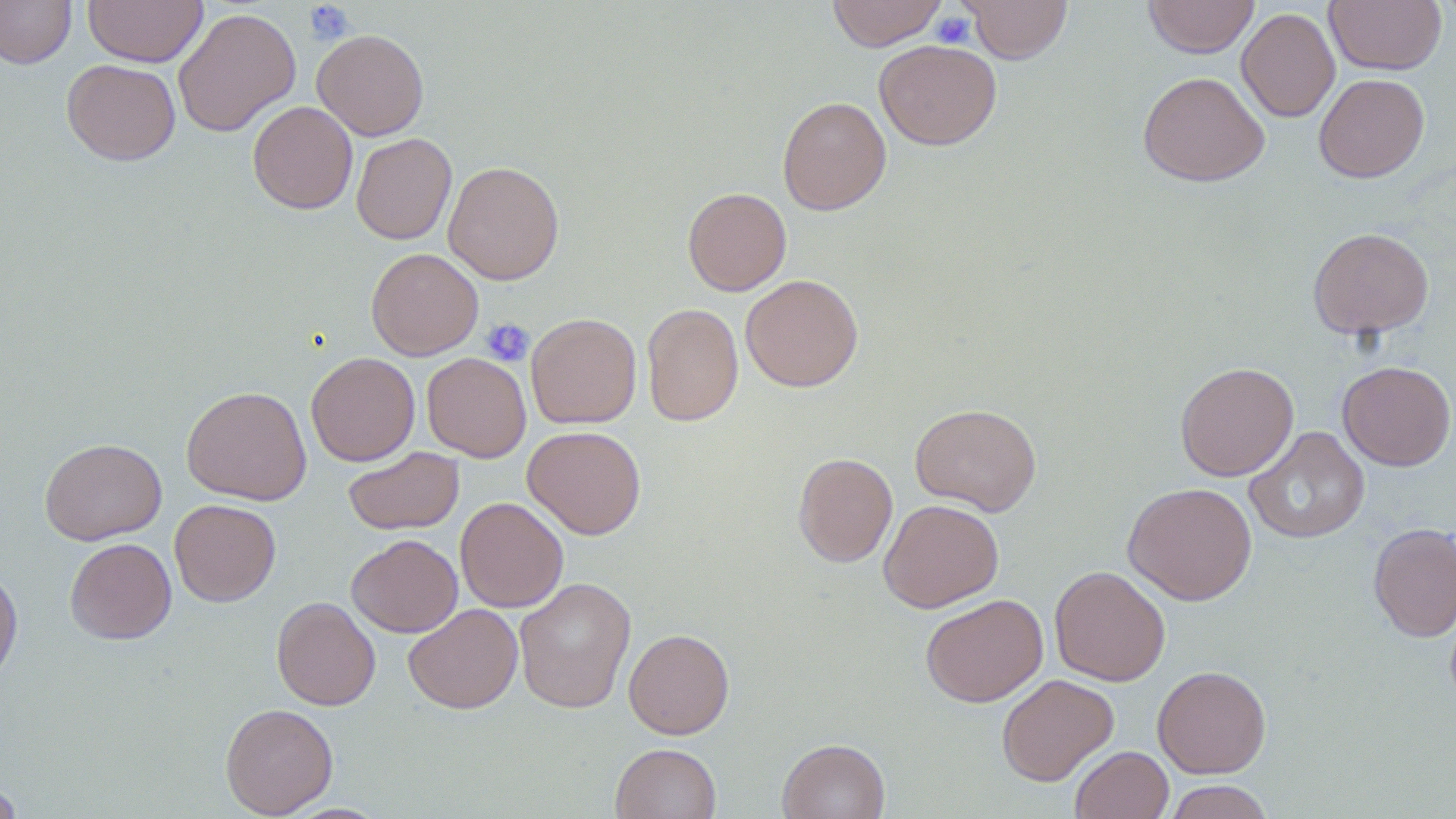
{
  "slide_level_diagnosis": "no evidence of blood parasites",
  "stain": "May-Grünwald-Giemsa",
  "image_size": "1456×819 pixels",
  "modality": "light microscopy",
  "magnification": "1000x",
  "platelet_locations": "approximate bounding boxes as named x1/y1/x2/y2 corners in pixels: (x1=304, y1=1, x2=355, y2=45), (x1=931, y1=11, x2=975, y2=48), (x1=480, y1=318, x2=535, y2=366)",
  "uninfected_red_blood_cell_locations": "approximate bounding boxes as named x1/y1/x2/y2 corners in pixels: (x1=0, y1=0, x2=76, y2=69), (x1=83, y1=0, x2=207, y2=67), (x1=826, y1=0, x2=946, y2=50), (x1=962, y1=0, x2=1073, y2=64), (x1=1142, y1=0, x2=1259, y2=58), (x1=1324, y1=0, x2=1447, y2=75), (x1=172, y1=7, x2=301, y2=137), (x1=1237, y1=7, x2=1340, y2=122), (x1=312, y1=29, x2=429, y2=141), (x1=874, y1=39, x2=1002, y2=151), (x1=62, y1=59, x2=181, y2=165), (x1=1137, y1=70, x2=1270, y2=187), (x1=1314, y1=73, x2=1430, y2=183), (x1=777, y1=96, x2=892, y2=215), (x1=247, y1=100, x2=358, y2=214), (x1=350, y1=133, x2=457, y2=245), (x1=443, y1=160, x2=565, y2=285), (x1=682, y1=187, x2=792, y2=296), (x1=1307, y1=226, x2=1434, y2=339), (x1=366, y1=248, x2=483, y2=360), (x1=740, y1=274, x2=863, y2=392), (x1=642, y1=303, x2=743, y2=426), (x1=525, y1=312, x2=642, y2=429), (x1=306, y1=352, x2=420, y2=466), (x1=422, y1=352, x2=531, y2=462), (x1=1175, y1=361, x2=1299, y2=481), (x1=1337, y1=361, x2=1456, y2=471), (x1=181, y1=385, x2=311, y2=505), (x1=910, y1=403, x2=1042, y2=516), (x1=523, y1=425, x2=646, y2=539), (x1=1245, y1=426, x2=1370, y2=544), (x1=39, y1=437, x2=167, y2=545), (x1=344, y1=446, x2=464, y2=535), (x1=793, y1=452, x2=898, y2=568), (x1=1123, y1=482, x2=1257, y2=606), (x1=455, y1=497, x2=568, y2=612), (x1=878, y1=498, x2=1004, y2=613), (x1=169, y1=499, x2=281, y2=606), (x1=1368, y1=521, x2=1456, y2=642), (x1=347, y1=534, x2=463, y2=637), (x1=64, y1=537, x2=176, y2=644), (x1=1049, y1=565, x2=1171, y2=686), (x1=0, y1=567, x2=23, y2=688), (x1=514, y1=576, x2=636, y2=714), (x1=920, y1=593, x2=1049, y2=707), (x1=271, y1=596, x2=381, y2=710), (x1=403, y1=603, x2=523, y2=714), (x1=624, y1=628, x2=734, y2=739), (x1=1152, y1=664, x2=1271, y2=778), (x1=996, y1=673, x2=1119, y2=786), (x1=220, y1=702, x2=338, y2=818), (x1=777, y1=738, x2=890, y2=819), (x1=610, y1=743, x2=721, y2=819), (x1=1070, y1=745, x2=1173, y2=818), (x1=0, y1=778, x2=24, y2=819), (x1=1162, y1=780, x2=1275, y2=819)",
  "field_of_view": "single",
  "preparation": "thin blood film"
}